Assess this cell for malaria.
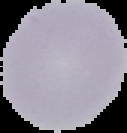
It is uninfected.

Summary:
  - Image type: cell region segmented out of the field of view; surrounding area masked to black
  - Preparation: thin blood smear
  - Image size: 127×133 pixels